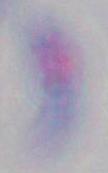
identification = Toxoplasma gondii
magnification = 1000x
modality = photomicrograph